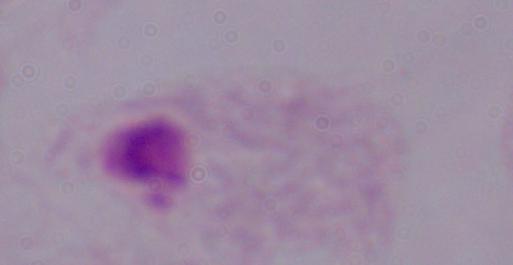
identification = trichomonad
modality = photomicrograph
magnification = 1000x